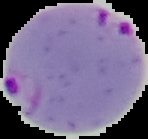 Image is 148×139 pixels. Result: Plasmodium parasites detected. Segmented cell region on a black background. From a thin blood smear.